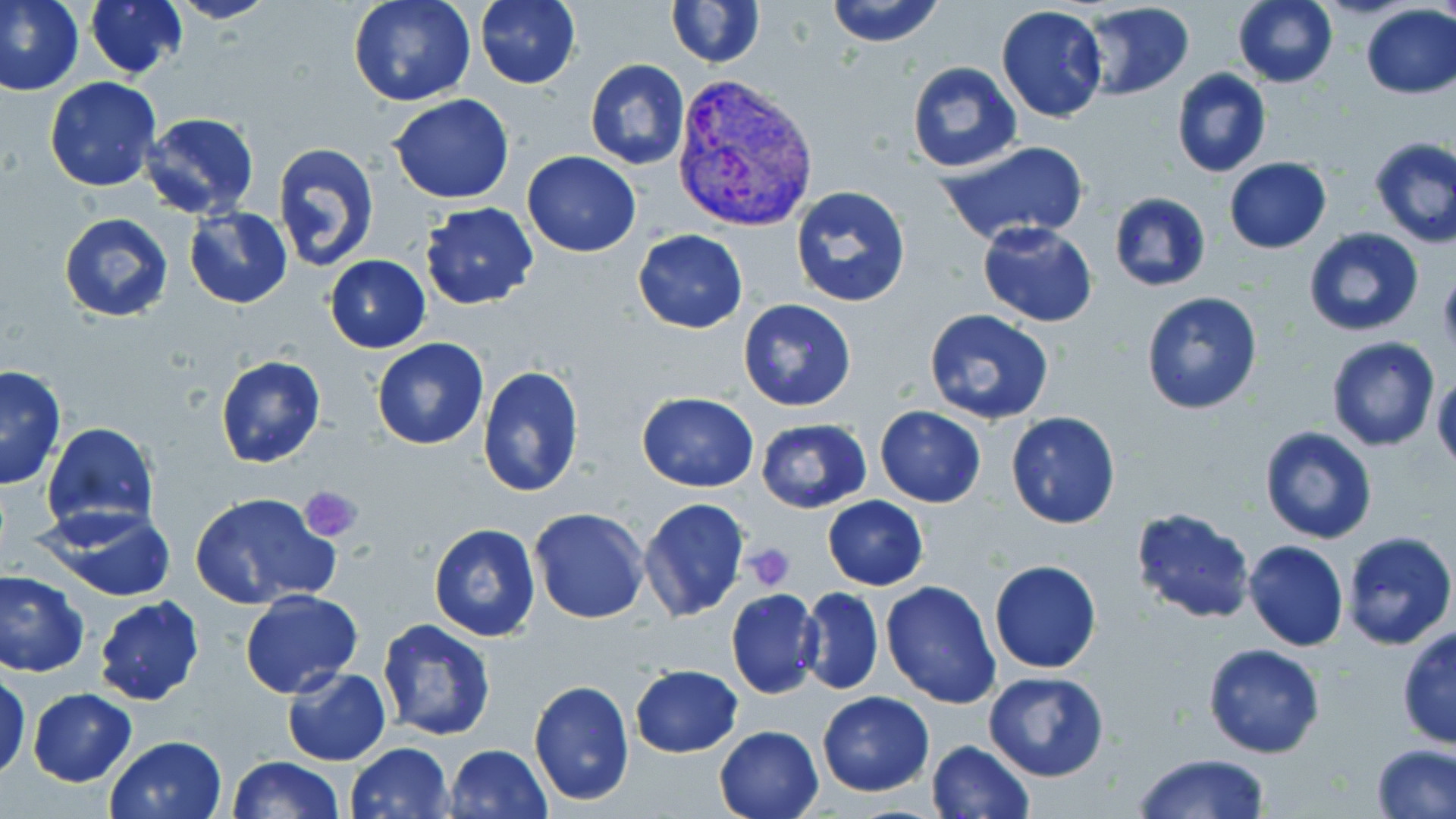

slide-level diagnosis = Plasmodium vivax
uninfected red blood cell locations = approximate bounding boxes as [x1, y1, x2, y2] in pixels: [0, 0, 84, 98], [85, 0, 189, 79], [167, 0, 281, 25], [349, 0, 474, 107], [474, 0, 581, 89], [666, 0, 765, 68], [823, 0, 946, 48], [1233, 0, 1338, 88], [1080, 2, 1195, 99], [1359, 4, 1456, 98], [995, 6, 1108, 124], [583, 58, 690, 169], [906, 61, 1022, 172], [1171, 68, 1272, 178], [43, 76, 162, 192], [388, 94, 515, 204], [138, 112, 261, 222], [1368, 136, 1456, 249], [934, 140, 1092, 246], [272, 141, 379, 273], [521, 151, 642, 257], [1224, 157, 1332, 253], [788, 185, 912, 308], [1109, 192, 1211, 292], [419, 201, 540, 309], [183, 208, 294, 309], [60, 214, 175, 323], [976, 222, 1099, 326], [1304, 227, 1425, 337], [633, 229, 747, 333], [324, 255, 430, 352], [1139, 290, 1264, 416], [736, 299, 858, 413], [923, 308, 1055, 424], [1325, 336, 1439, 451], [372, 339, 489, 450], [216, 355, 326, 468], [0, 366, 66, 490], [477, 366, 585, 499], [1432, 369, 1456, 473], [638, 392, 759, 490], [874, 406, 987, 507], [1005, 411, 1121, 528], [755, 419, 872, 513], [41, 422, 159, 534], [1259, 426, 1379, 545], [189, 491, 339, 609], [822, 495, 928, 590], [638, 497, 750, 622], [26, 503, 179, 603], [1130, 505, 1256, 624], [528, 507, 650, 624], [429, 523, 540, 641], [1341, 531, 1456, 649], [1243, 540, 1349, 651], [988, 559, 1101, 673], [0, 570, 89, 678], [881, 580, 1002, 707], [798, 587, 884, 696], [726, 588, 823, 700], [240, 589, 362, 696], [92, 595, 205, 706], [376, 618, 496, 741], [1395, 627, 1456, 749], [1203, 643, 1326, 759], [629, 664, 743, 758], [282, 667, 392, 766], [983, 670, 1109, 782], [1, 671, 29, 781], [528, 678, 634, 806], [27, 688, 137, 787], [817, 691, 934, 796], [715, 724, 825, 818], [104, 734, 227, 819], [926, 740, 1035, 819], [345, 742, 454, 819], [444, 742, 552, 819], [1372, 743, 1456, 819], [1131, 753, 1271, 819], [226, 756, 346, 818]
field of view = single
magnification = 1000x
Plasmodium vivax-infected red blood cell locations = approximate bounding boxes as [x1, y1, x2, y2] in pixels: [670, 74, 821, 231]
image size = 1456×819 pixels
preparation = thin blood film
stain = May-Grünwald-Giemsa
platelet locations = approximate bounding boxes as [x1, y1, x2, y2] in pixels: [1436, 268, 1456, 351], [301, 485, 362, 544], [745, 542, 797, 590]
modality = light microscopy